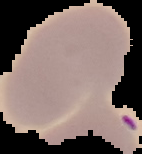
Cell region segmented out of the field of view; the surrounding area is masked to black. From a thin blood smear. Result: negative for Plasmodium parasites. Image is 142×154 pixels.